Name the parasite shown.
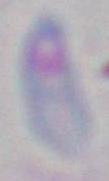
This is Toxoplasma gondii.

modality = micrograph
magnification = 1000x